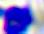
Summary:
  - Modality: micrograph
  - Identification: leukocyte
  - Magnification: 400x